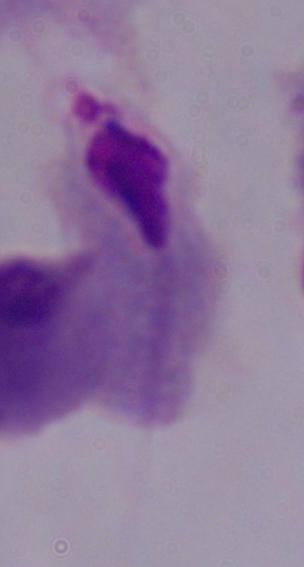

magnification = 1000x
identification = trichomonad
modality = photomicrograph